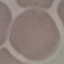 Malaria status: uninfected. Thin smear of blood. Giemsa-stained preparation. Automatically extracted cell patch, resized to 64 × 64 pixels. Photographed with a smartphone camera at the microscope eyepiece.